Classify this cell by malaria status.
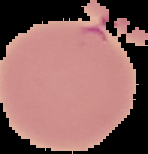
Parasitized.

Summary:
  - Preparation: thin blood film
  - Image type: segmented cell region with the area outside set to black
  - Image size: 148×154 pixels